Outline each blood parasite and name the species.
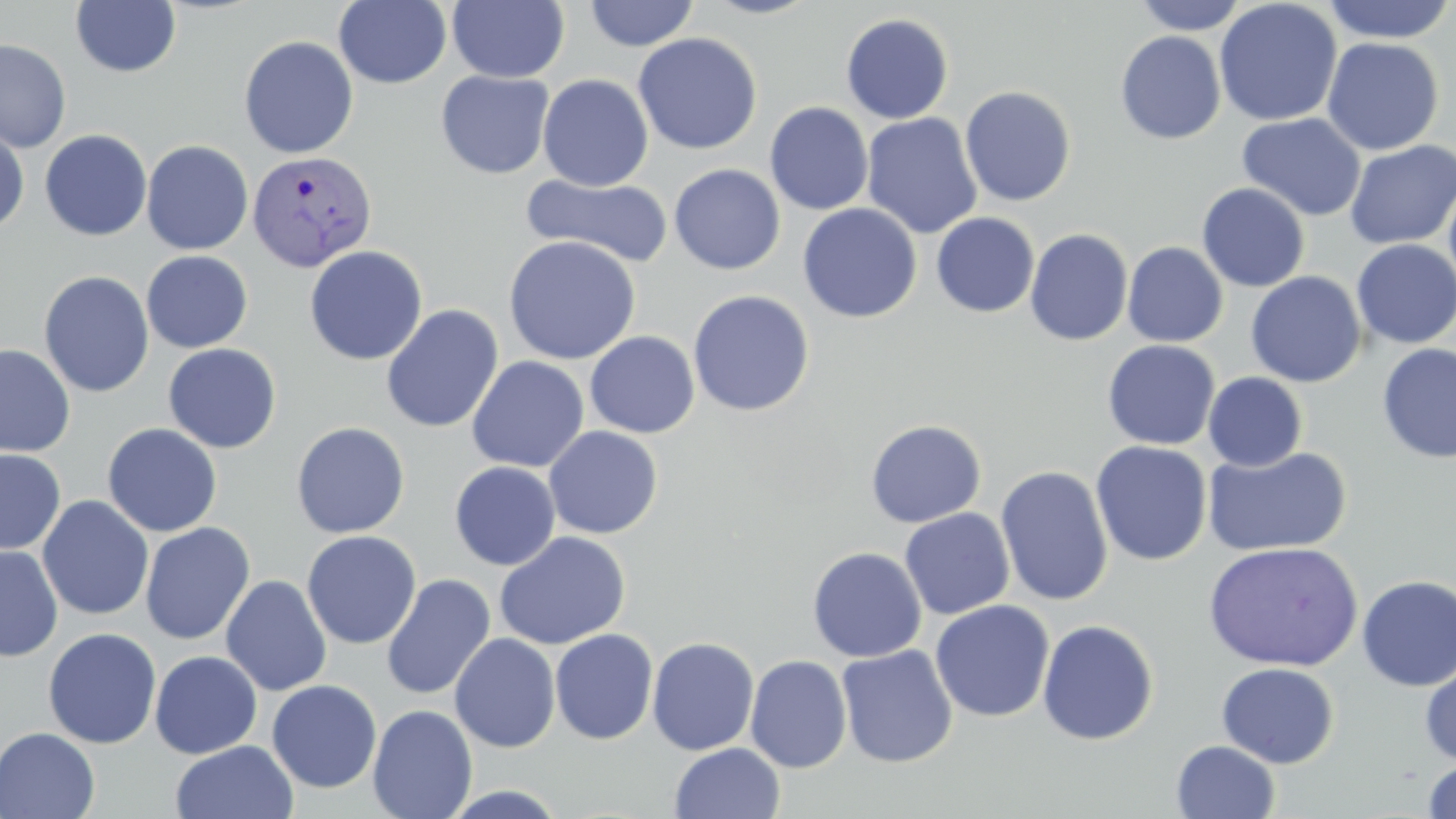
Approximate bounding boxes as (x1, y1, x2, y2) in pixels.
Plasmodium vivax-infected red blood cells: (247, 150, 377, 272).
No Plasmodium falciparum, Plasmodium ovale, Plasmodium malariae, Babesia divergens, or Trypanosoma brucei observed.

Uninfected red blood cell locations: (447, 0, 569, 83), (698, 0, 824, 19), (1132, 0, 1250, 35), (1320, 0, 1456, 44), (70, 1, 182, 78), (333, 1, 453, 89), (583, 1, 700, 51), (1214, 1, 1342, 127), (840, 13, 954, 124), (1115, 31, 1226, 144), (633, 32, 763, 155), (239, 35, 359, 159), (1321, 37, 1444, 156), (0, 39, 71, 153), (435, 70, 555, 179), (537, 74, 654, 191), (959, 86, 1076, 206), (765, 102, 873, 215), (1237, 112, 1366, 221), (861, 113, 983, 239), (0, 126, 30, 234), (39, 129, 152, 242), (141, 140, 254, 255), (1344, 140, 1456, 249), (669, 164, 785, 275), (1442, 170, 1456, 302), (520, 173, 674, 268), (1197, 183, 1310, 292), (798, 203, 922, 323), (931, 212, 1040, 318), (1024, 228, 1133, 346), (503, 235, 641, 365), (1352, 239, 1456, 349), (1122, 241, 1228, 347), (304, 245, 428, 365), (141, 250, 253, 353), (38, 270, 155, 398), (1246, 271, 1367, 388), (687, 290, 815, 417), (380, 304, 504, 433), (584, 331, 700, 438), (1102, 340, 1221, 450), (0, 343, 75, 457), (163, 343, 282, 454), (1376, 343, 1456, 463), (466, 356, 589, 473), (1203, 372, 1308, 471), (865, 419, 986, 528), (291, 422, 410, 539), (103, 423, 222, 537), (543, 425, 663, 539), (1090, 441, 1212, 566), (1202, 445, 1352, 557), (0, 448, 66, 555), (449, 461, 561, 570), (995, 465, 1114, 606), (37, 496, 154, 620), (899, 508, 1015, 620), (139, 522, 255, 645), (302, 531, 421, 649), (494, 531, 631, 651), (1203, 541, 1363, 671), (0, 545, 63, 662), (807, 547, 927, 662), (381, 574, 496, 701), (1356, 574, 1456, 691), (221, 575, 332, 696), (929, 600, 1055, 722), (1037, 619, 1159, 745), (43, 628, 162, 749), (550, 628, 659, 745), (449, 633, 561, 753), (647, 637, 760, 755), (836, 645, 958, 768), (149, 650, 263, 759), (745, 654, 853, 773), (1419, 657, 1456, 767), (1215, 662, 1339, 768), (266, 680, 382, 793), (367, 704, 478, 819), (0, 728, 100, 819), (170, 740, 299, 819), (1171, 740, 1280, 819), (670, 743, 785, 819), (1422, 759, 1456, 818), (437, 784, 571, 818). Slide-level diagnosis: Plasmodium vivax. Captured at 1000x magnification. May-Grünwald-Giemsa stain. Light microscopy. Thin blood film. Image is 1456×819 pixels. Single field of view.